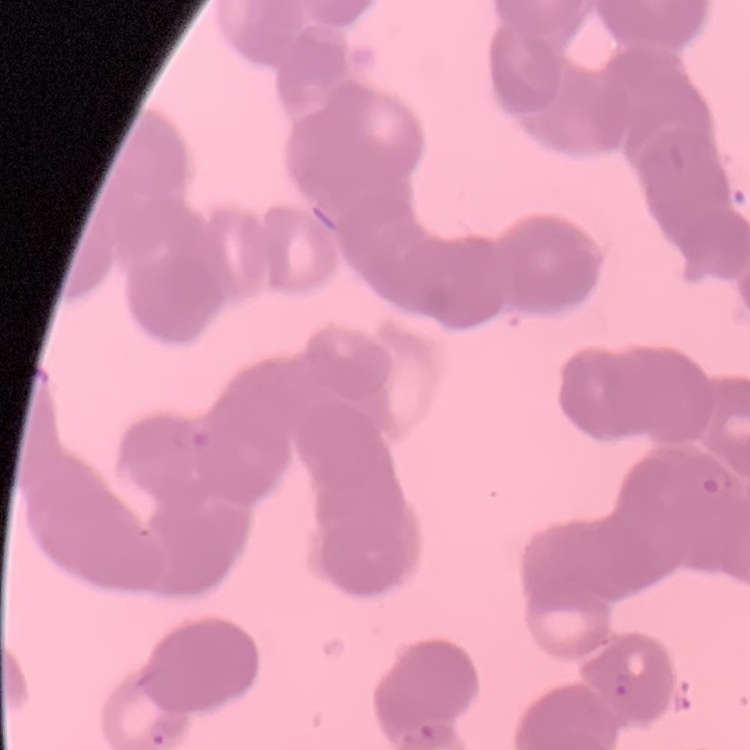

The erythrocytes exhibit rouleaux formation. One tile cut from a larger photomicrograph. Stained with either Field's or Giemsa. Thin peripheral smear.